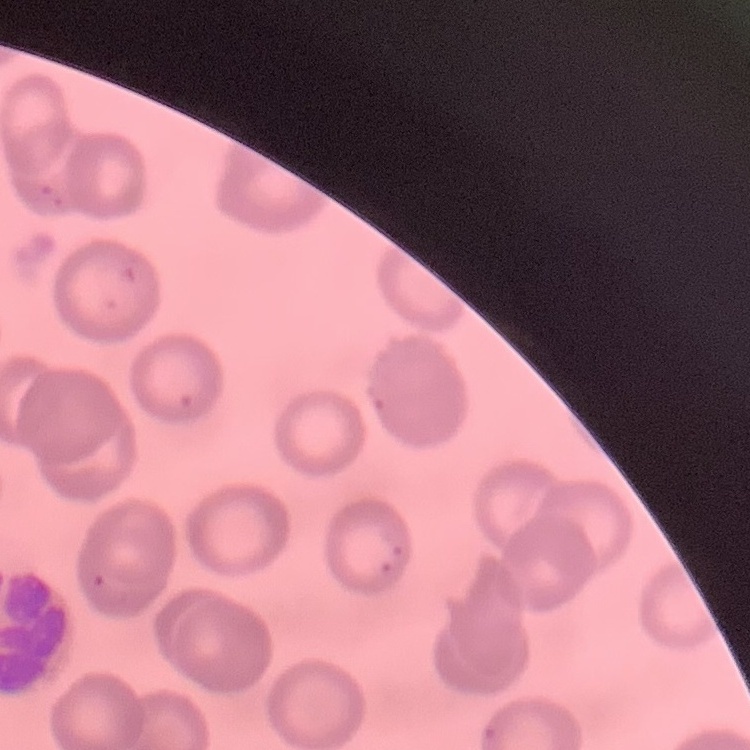

{
  "erythrocyte_morphology": "no rouleaux formation",
  "preparation": "thin blood film",
  "image_type": "square crop of a larger photomicrograph",
  "stain": "Field's or Giemsa"
}